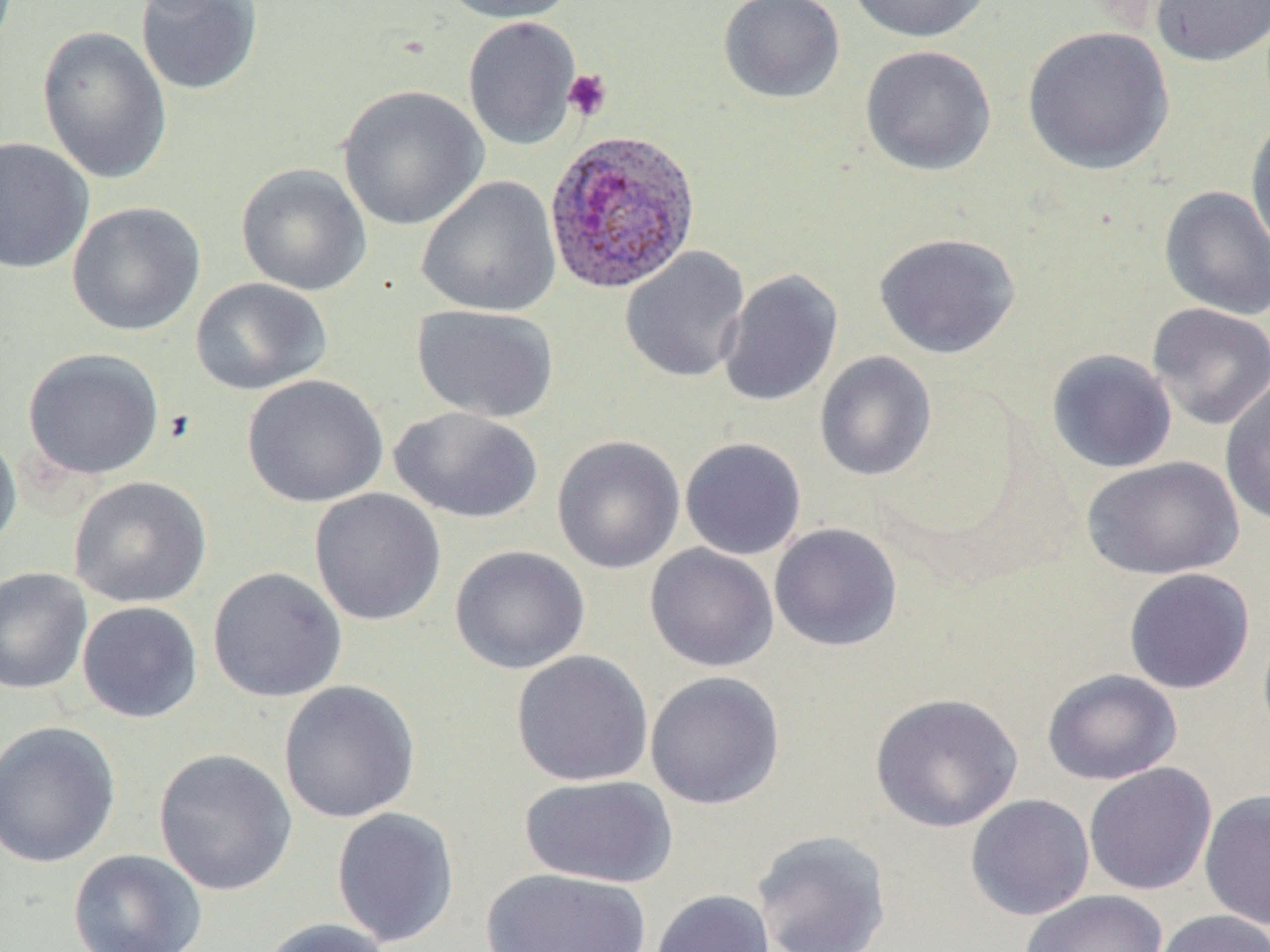

Approximate bounding boxes as (x1, y1, x2, y2) in pixels. Platelet locations: (562, 69, 613, 121). Uninfected red blood cell locations: (436, 0, 577, 23), (717, 0, 845, 104), (846, 0, 993, 43), (1151, 0, 1270, 67), (135, 1, 264, 96), (463, 16, 582, 150), (1021, 25, 1175, 176), (36, 26, 172, 185), (859, 44, 997, 177), (337, 84, 489, 231), (1245, 115, 1270, 257), (0, 137, 95, 274), (235, 163, 373, 297), (416, 176, 561, 318), (1159, 185, 1270, 321), (66, 201, 206, 337), (873, 232, 1021, 359), (620, 246, 751, 382), (719, 269, 843, 407), (189, 277, 331, 396), (1146, 303, 1270, 430), (412, 304, 559, 423), (22, 347, 164, 481), (1046, 348, 1178, 474), (814, 351, 937, 481), (242, 373, 389, 508), (1220, 378, 1270, 527), (389, 406, 543, 524), (0, 426, 23, 556), (552, 435, 685, 574), (679, 436, 807, 561), (1080, 456, 1244, 580), (68, 476, 212, 609), (309, 488, 447, 627), (769, 522, 903, 653), (644, 544, 779, 672), (449, 545, 590, 675), (206, 566, 348, 703), (0, 567, 92, 695), (1123, 567, 1256, 694), (77, 601, 203, 723), (511, 649, 654, 787), (1042, 668, 1182, 785), (645, 671, 785, 810), (278, 680, 421, 824), (869, 692, 1024, 832), (0, 720, 121, 869), (152, 747, 298, 896), (1084, 762, 1217, 896), (519, 774, 678, 888), (1199, 789, 1270, 930), (965, 794, 1095, 920), (330, 806, 460, 948), (751, 829, 893, 952), (68, 848, 208, 952), (479, 867, 652, 951), (650, 889, 774, 952), (1021, 889, 1168, 952), (1151, 909, 1269, 952), (256, 917, 395, 952). Plasmodium ovale-infected red blood cell locations: (542, 129, 702, 295). Slide-level diagnosis: Plasmodium ovale. Optical microscopy. May-Grünwald-Giemsa stain. Single field of view. Image is 1270×952 pixels. Thin blood smear. Captured at 1000x magnification.